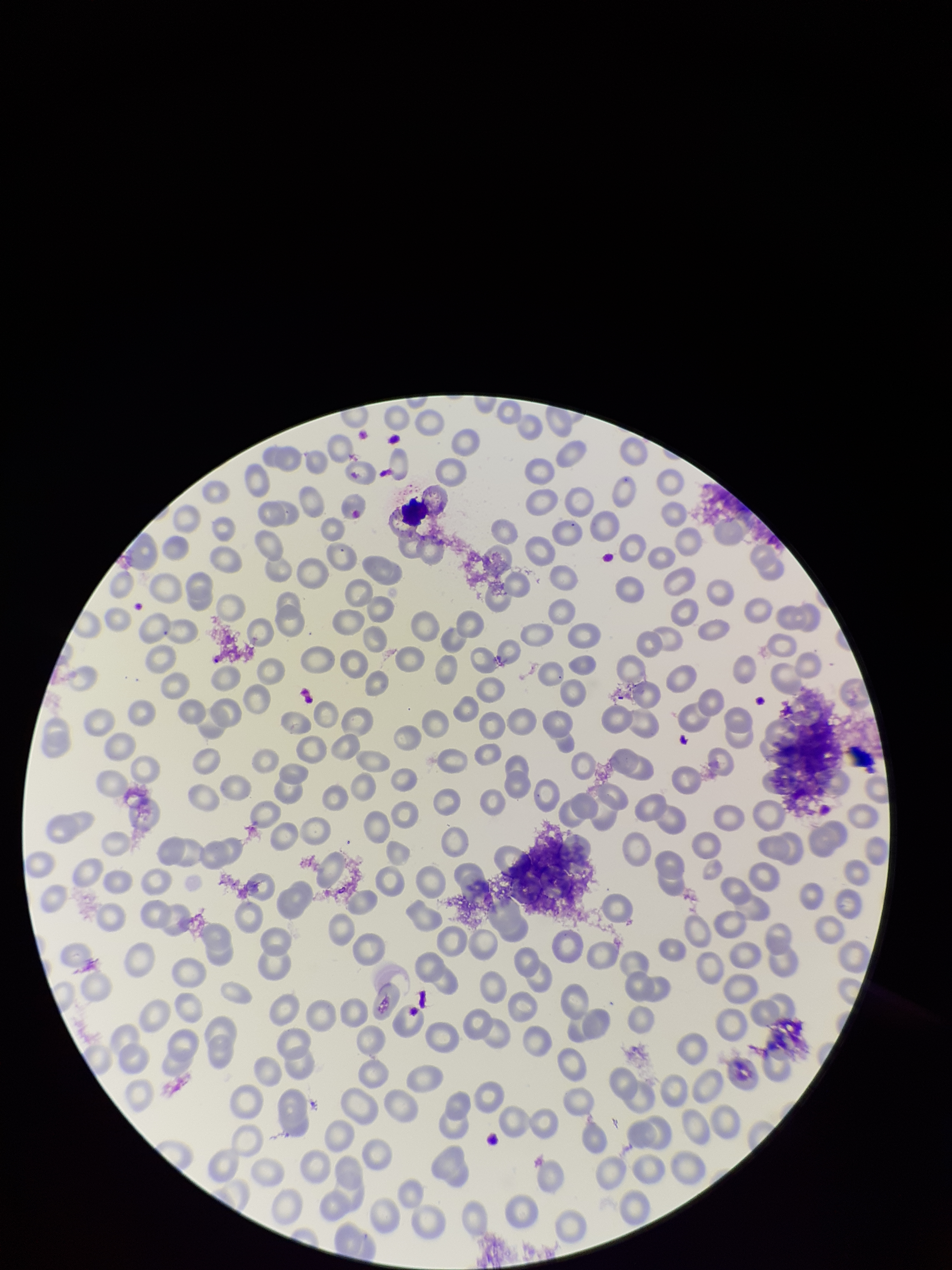

parasitized red blood cells = none seen
parasitized red blood cell count = 0
field of view = single
preparation = thin smear
capture = smartphone photograph through the microscope eyepiece
red blood cell count = 230
patient malaria status = infected
stain = Giemsa
species reported for this patient = Plasmodium falciparum
image size = 952×1270 pixels